Assess this cell for malaria.
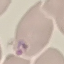
It is parasitized.

preparation = thin blood smear
capture = smartphone camera at the microscope eyepiece
image type = cell patch, automatically extracted from a larger field of view and resized to 64 × 64 pixels
stain = Giemsa